Assess this cell for malaria.
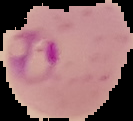

Parasitized.

From a thin blood film. Image is 133×121 pixels. Cell region segmented out of the field of view; the surrounding area is masked to black.